Locate every Plasmodium ovale-infected red blood cell.
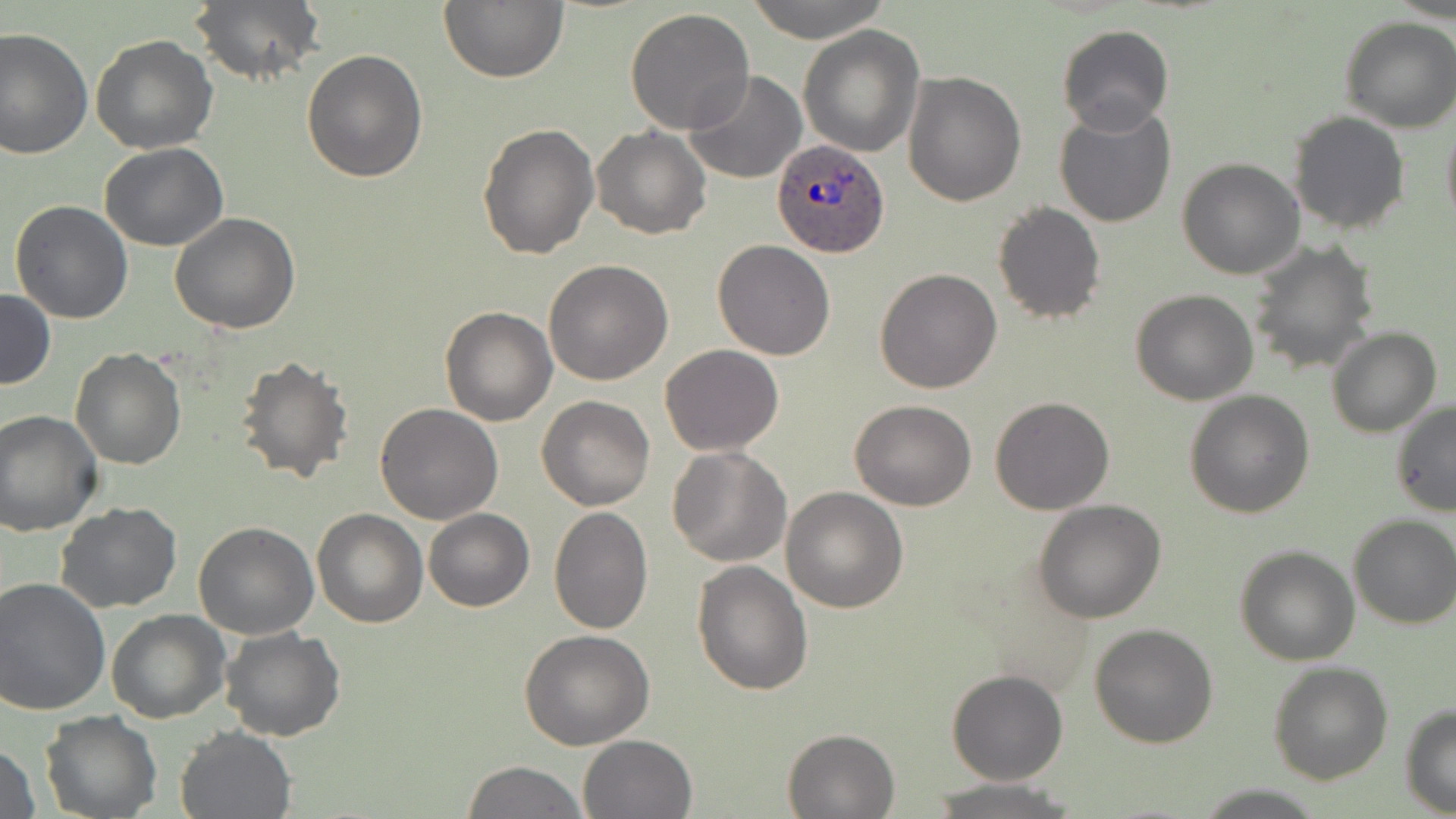

Approximate bounding boxes as [x1, y1, x2, y2] in pixels.
Plasmodium ovale-infected red blood cells: [773, 141, 888, 258].

Uninfected red blood cell locations: [188, 0, 326, 88], [438, 0, 567, 83], [745, 0, 890, 43], [624, 8, 755, 135], [1339, 18, 1455, 133], [1056, 25, 1174, 134], [799, 26, 926, 157], [0, 28, 93, 158], [89, 34, 219, 154], [300, 48, 428, 183], [682, 71, 808, 186], [902, 71, 1026, 206], [1053, 104, 1176, 228], [1288, 110, 1409, 235], [1441, 113, 1456, 236], [477, 121, 600, 260], [591, 127, 710, 240], [100, 141, 228, 251], [1177, 158, 1305, 279], [9, 200, 134, 324], [992, 200, 1106, 323], [170, 212, 301, 333], [712, 240, 836, 360], [1248, 240, 1380, 375], [543, 260, 674, 385], [874, 268, 1002, 394], [0, 289, 55, 389], [1130, 290, 1259, 406], [438, 306, 557, 425], [1326, 327, 1442, 438], [659, 344, 783, 456], [70, 347, 186, 470], [236, 354, 357, 487], [1184, 390, 1314, 518], [537, 395, 654, 510], [988, 397, 1114, 516], [849, 400, 978, 511], [1390, 400, 1456, 518], [375, 403, 503, 524], [0, 410, 102, 535], [668, 446, 793, 566], [780, 486, 909, 613], [1034, 500, 1167, 622], [57, 503, 182, 613], [549, 506, 653, 635], [423, 508, 535, 613], [313, 509, 427, 627], [1347, 513, 1456, 630], [193, 521, 319, 639], [1234, 544, 1360, 665], [691, 560, 815, 696], [0, 577, 111, 716], [106, 610, 230, 722], [1090, 624, 1218, 748], [220, 627, 347, 743], [519, 629, 656, 749], [1269, 661, 1395, 786], [946, 671, 1067, 786], [1400, 704, 1456, 816], [40, 712, 161, 818], [174, 725, 296, 818], [782, 727, 899, 818], [579, 733, 696, 818], [0, 741, 41, 819], [460, 761, 586, 818], [923, 779, 1081, 818]. Slide-level diagnosis: Plasmodium ovale. Thin blood smear. Single field of view. May-Grünwald-Giemsa-stained preparation. Optical microscopy. Image is 1456×819 pixels. 1000x magnification.